Look for Plasmodium parasites.
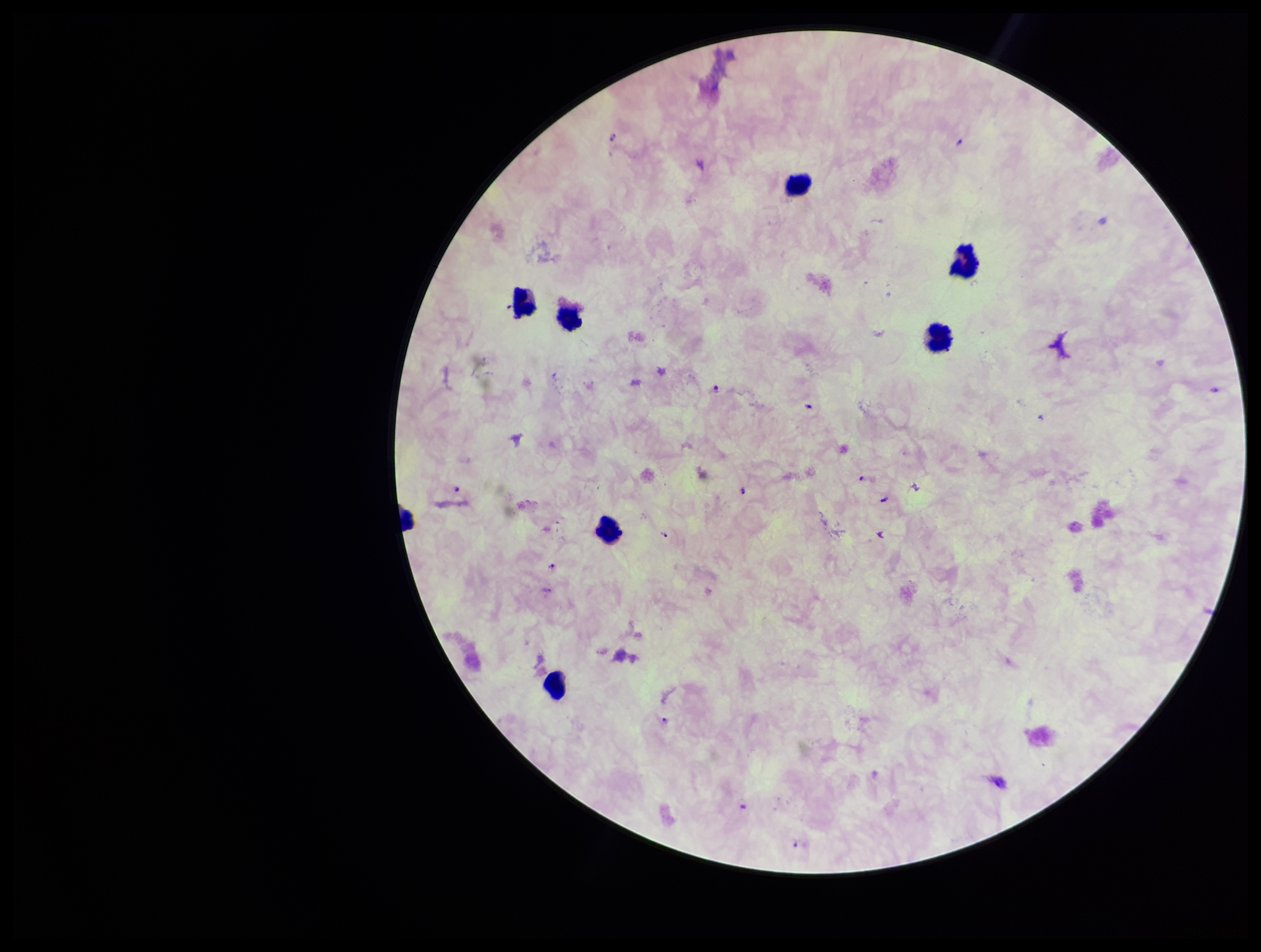
Seen.

{
  "patient_malaria_status": "infected",
  "capture": "smartphone photograph through the microscope eyepiece",
  "field_of_view": "one from this slide",
  "species_reported_for_this_patient": "Plasmodium falciparum",
  "image_size": "1261×952 pixels",
  "leukocyte_count": 6,
  "stain": "Giemsa",
  "parasite_count": 6,
  "preparation": "thick smear"
}